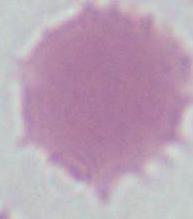 Photomicrograph. A red blood cell is seen. Captured at 1000x magnification.